Identify the parasite.
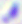

This is Toxoplasma gondii.

magnification = 400x
modality = photomicrograph